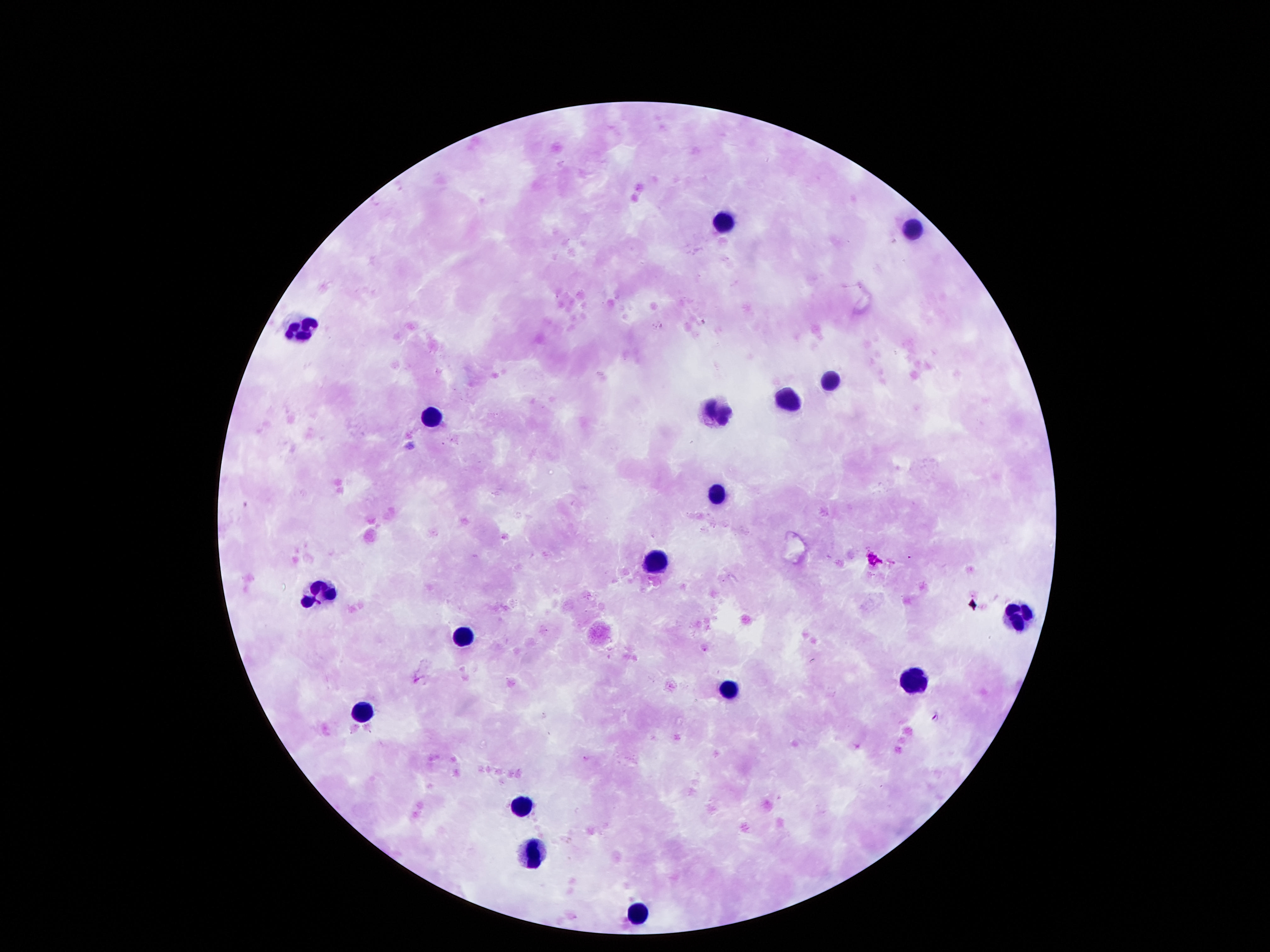

Approximate object centers, in pixels from the top-left corner. Leukocyte locations: (x=717, y=220), (x=908, y=227), (x=304, y=327), (x=834, y=376), (x=782, y=398), (x=721, y=411), (x=430, y=414), (x=714, y=492), (x=656, y=559), (x=320, y=588), (x=1015, y=608), (x=456, y=636), (x=911, y=681), (x=727, y=688), (x=365, y=708), (x=517, y=802), (x=530, y=847), (x=637, y=908). Image is 1270×952 pixels. 100x magnification. Patient malaria status: uninfected. Thick blood smear. One field from this slide. Photographed through the microscope eyepiece with a smartphone camera. Giemsa-stained preparation.